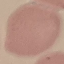

Malaria status: uninfected. Photographed with a smartphone camera at the microscope eyepiece. Thin blood smear. Automatically extracted cell patch, resized to 64 × 64 pixels. Giemsa-stained preparation.